Assess this cell for malaria.
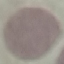
Uninfected.

Summary:
  - Preparation: thin blood film
  - Image type: cell patch, automatically extracted from a larger field of view and resized to 64 × 64 pixels
  - Stain: Giemsa
  - Capture: smartphone camera at the microscope eyepiece